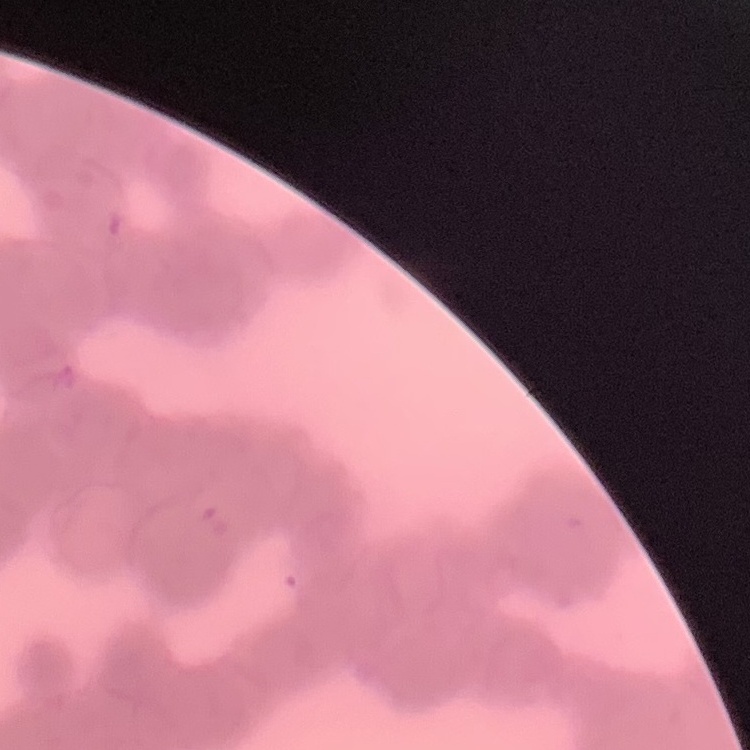
Summary:
  - Red blood cell morphology: rouleaux formation
  - Preparation: thin blood smear
  - Image type: square crop of a larger photomicrograph
  - Stain: Field's or Giemsa